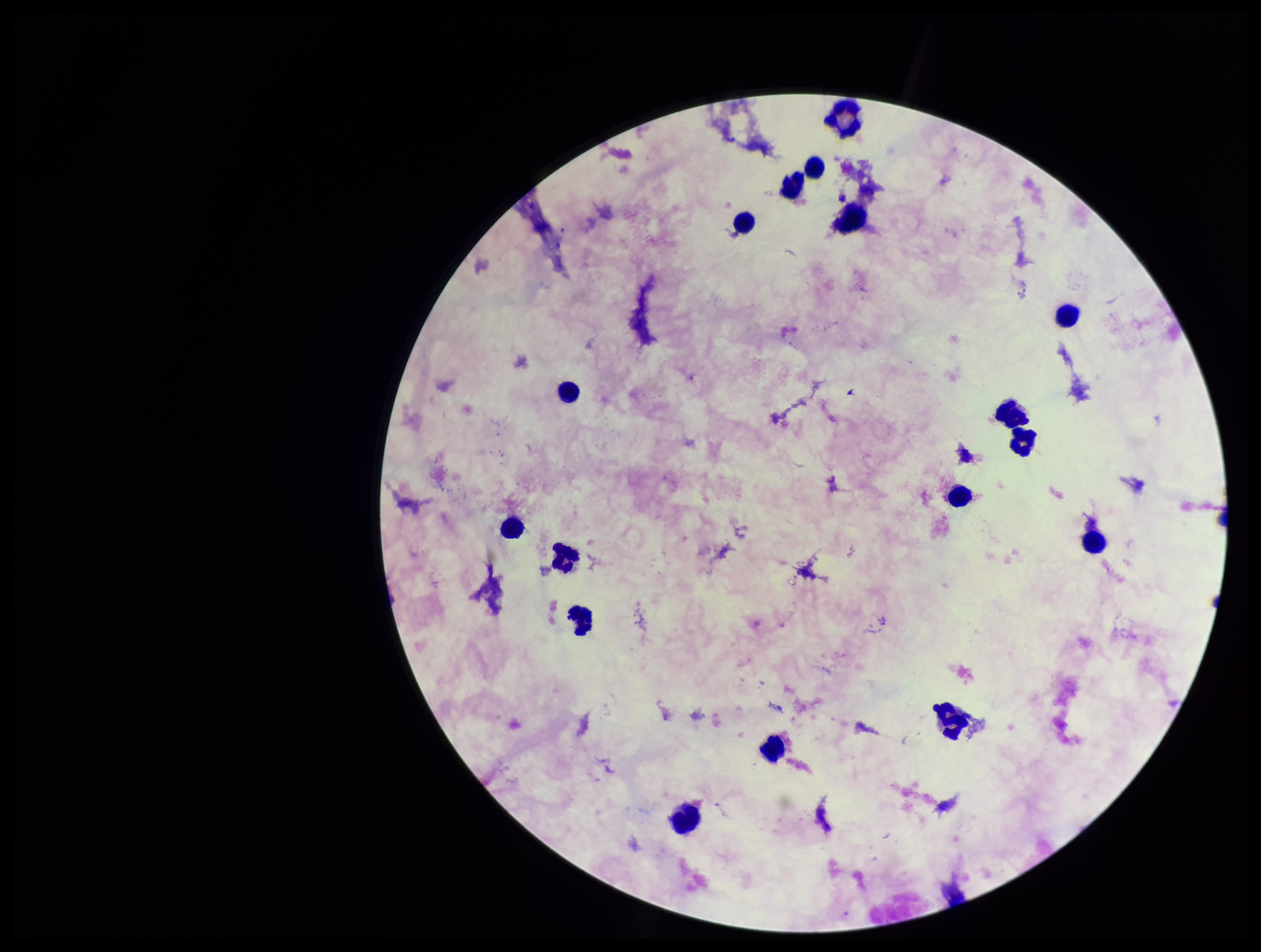
image_size: 1261×952 pixels
plasmodium_parasites: none detected
preparation: thick blood smear
parasite_count: 0
capture: smartphone photograph through the microscope eyepiece
patient_malaria_status: negative
stain: Giemsa
leukocyte_count: 17
field_of_view: one from this slide